Name the parasite shown.
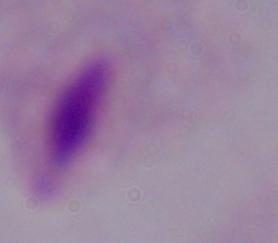

This is a trichomonad.

Captured at 1000x magnification. Photomicrograph.